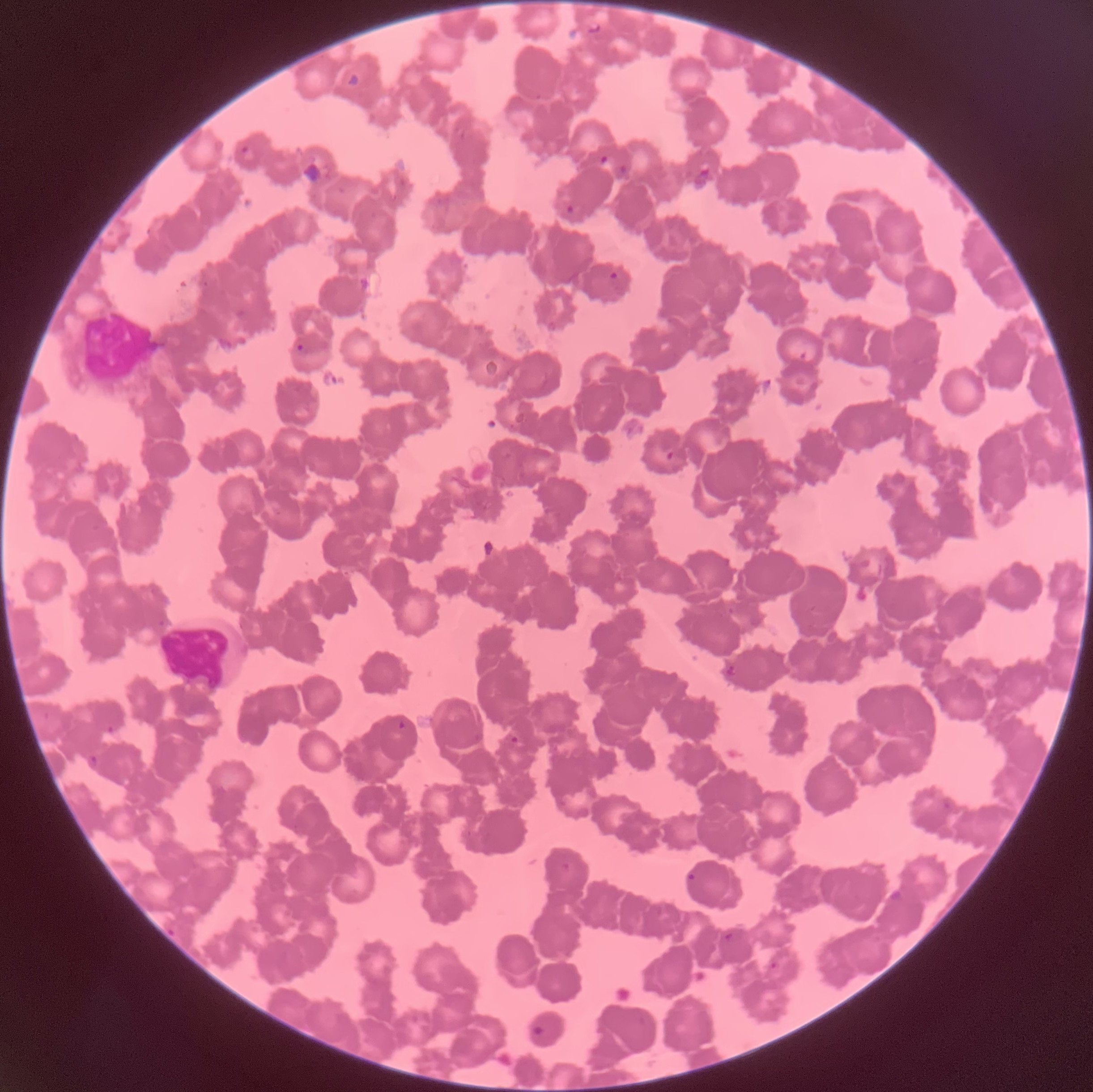
Approximate bounding boxes as [x1, y1, x2, y2] in pixels. White blood cell locations: [79, 307, 160, 385], [155, 616, 233, 688]. Plasmodium parasite locations: [239, 145, 256, 163], [598, 155, 611, 166], [617, 164, 632, 178], [694, 168, 712, 189], [565, 203, 577, 215], [608, 270, 620, 282], [296, 344, 305, 353], [665, 450, 675, 461], [724, 663, 737, 676], [397, 720, 408, 731], [105, 725, 116, 736], [510, 735, 519, 746], [87, 754, 98, 769], [686, 871, 696, 885], [723, 932, 736, 942], [769, 961, 779, 970], [531, 1023, 545, 1037]. Thin blood film. Image is 1093×1092 pixels. Optical microscopy. The red blood cells show rouleaux formation.